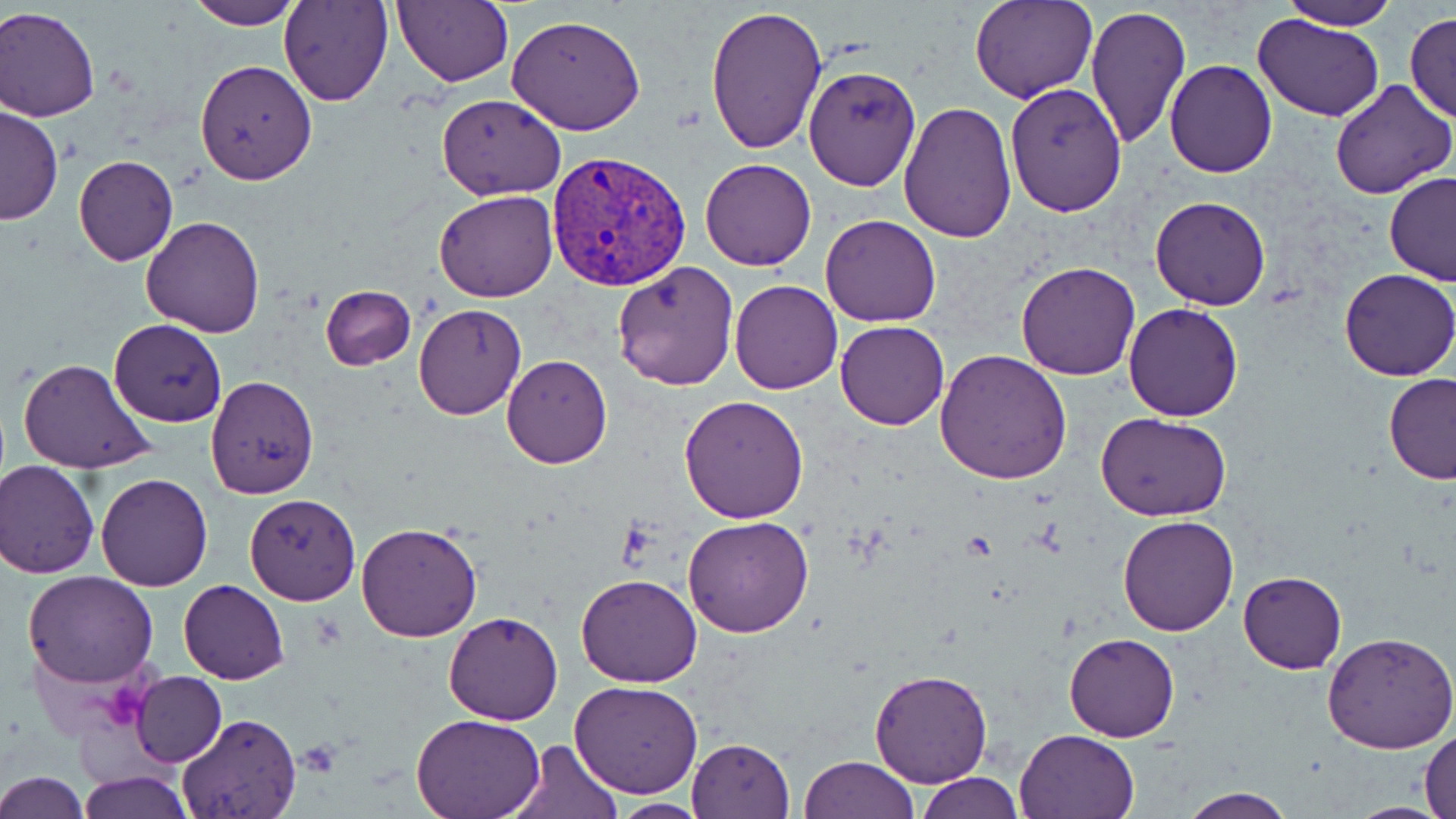

Summary:
  - Coordinate format: approximate bounding boxes as [x1, y1, x2, y2] in pixels
  - Plasmodium vivax-infected red blood cell locations: [544, 149, 693, 289]
  - Uninfected red blood cell locations: [185, 0, 305, 29], [280, 0, 393, 106], [969, 0, 1095, 102], [1277, 0, 1400, 31], [392, 1, 513, 88], [1085, 2, 1190, 149], [0, 4, 101, 122], [703, 4, 827, 155], [1404, 11, 1455, 125], [1252, 13, 1386, 124], [506, 16, 646, 136], [194, 59, 319, 184], [1164, 60, 1277, 177], [802, 65, 921, 191], [1330, 81, 1456, 200], [1004, 82, 1127, 216], [436, 94, 565, 200], [897, 100, 1018, 243], [1, 106, 61, 227], [73, 154, 179, 266], [700, 159, 818, 270], [1384, 172, 1455, 287], [434, 188, 558, 302], [1150, 195, 1271, 310], [820, 213, 943, 327], [141, 214, 267, 336], [612, 260, 741, 391], [1014, 260, 1142, 381], [1340, 268, 1456, 381], [730, 280, 843, 394], [320, 285, 416, 371], [413, 302, 527, 420], [1123, 303, 1246, 421], [109, 319, 227, 426], [835, 320, 949, 429], [936, 347, 1072, 485], [502, 355, 612, 469], [17, 357, 157, 475], [1382, 373, 1456, 485], [205, 375, 319, 498], [679, 394, 809, 522], [1096, 413, 1230, 521], [0, 459, 99, 577], [95, 473, 213, 591], [244, 494, 360, 605], [684, 514, 815, 638], [1117, 515, 1240, 636], [356, 522, 484, 643], [1238, 570, 1346, 674], [23, 571, 159, 688], [575, 572, 702, 687], [179, 580, 289, 684], [444, 612, 563, 725], [1324, 632, 1456, 754], [1064, 633, 1180, 741], [869, 668, 994, 788], [130, 672, 226, 766], [571, 680, 702, 798], [175, 713, 303, 819], [411, 713, 546, 819], [1015, 728, 1139, 818], [1419, 728, 1456, 819], [686, 737, 795, 819], [509, 738, 620, 819], [798, 756, 919, 819], [77, 769, 194, 819], [0, 770, 90, 818], [915, 773, 1025, 818], [1175, 788, 1297, 819], [605, 799, 717, 818], [1342, 801, 1452, 818]
  - Platelet locations: [294, 742, 343, 777]
  - Slide-level diagnosis: Plasmodium vivax
  - Stain: May-Grünwald-Giemsa
  - Preparation: thin blood smear
  - Magnification: 1000x
  - Image size: 1456×819 pixels
  - Modality: optical microscopy
  - Field of view: single